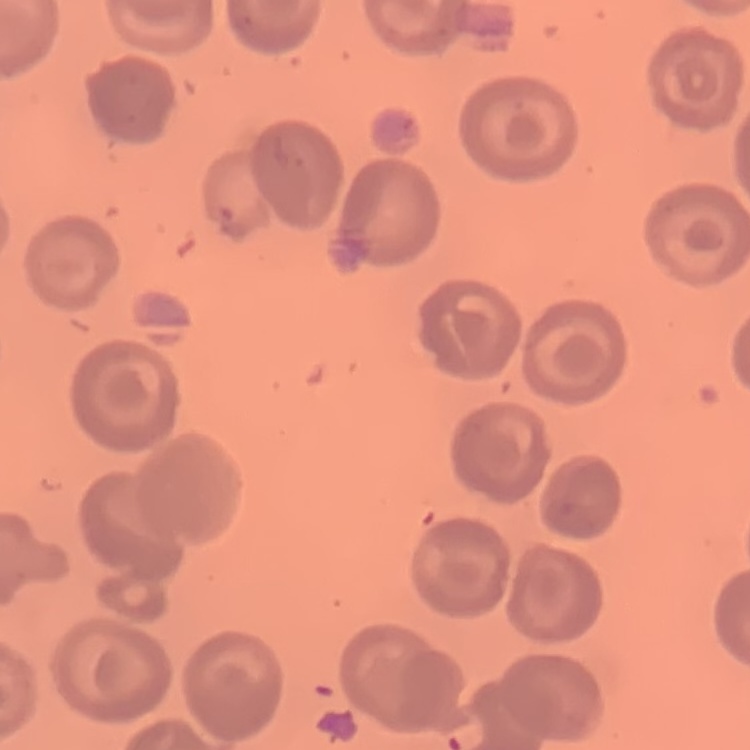
Summary:
  - Red blood cell morphology: no rouleaux formation
  - Preparation: thin blood film
  - Stain: Field's or Giemsa
  - Image type: square crop of a larger photomicrograph